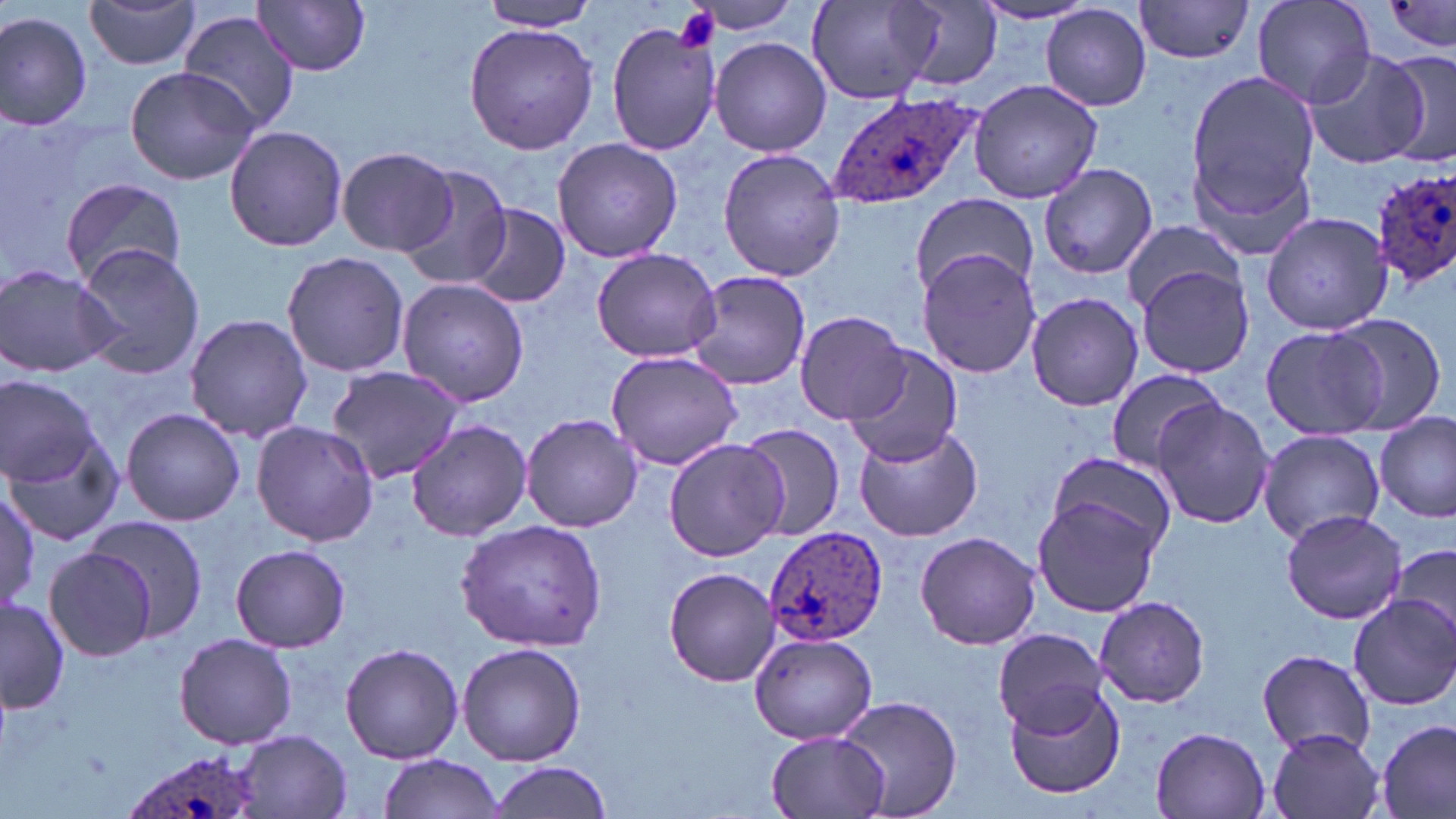 Approximate bounding boxes as (x1, y1, x2, y2) in pixels. Plasmodium ovale-infected red blood cell locations: (826, 89, 981, 213), (1373, 168, 1456, 285), (762, 524, 889, 646), (119, 746, 268, 819). Platelet locations: (675, 6, 721, 53). Uninfected red blood cell locations: (82, 0, 203, 70), (807, 0, 943, 106), (1134, 0, 1255, 64), (1252, 0, 1377, 108), (255, 1, 372, 75), (1381, 1, 1456, 51), (475, 2, 604, 31), (680, 2, 809, 37), (896, 2, 1004, 94), (973, 2, 1096, 25), (1041, 4, 1152, 111), (0, 8, 95, 131), (179, 9, 300, 135), (464, 23, 598, 156), (608, 23, 719, 156), (710, 36, 833, 157), (1300, 46, 1430, 168), (1379, 47, 1456, 162), (122, 64, 262, 186), (1185, 67, 1320, 219), (969, 77, 1104, 205), (223, 125, 347, 251), (551, 136, 684, 263), (336, 146, 457, 257), (718, 148, 846, 283), (395, 163, 514, 291), (1039, 164, 1158, 279), (59, 176, 188, 290), (909, 191, 1039, 299), (465, 203, 569, 309), (1261, 210, 1395, 335), (1120, 218, 1245, 315), (70, 243, 209, 381), (590, 247, 722, 363), (918, 249, 1042, 378), (282, 250, 409, 379), (0, 264, 121, 379), (1136, 265, 1253, 379), (683, 268, 812, 392), (397, 279, 529, 408), (1026, 290, 1143, 411), (795, 309, 912, 423), (184, 313, 313, 444), (1330, 314, 1450, 433), (1259, 323, 1390, 441), (843, 346, 963, 467), (606, 351, 742, 469), (326, 364, 464, 484), (1103, 369, 1226, 473), (1, 376, 100, 484), (1150, 399, 1275, 530), (121, 408, 245, 527), (521, 413, 643, 532), (1375, 413, 1455, 522), (404, 419, 533, 541), (252, 421, 379, 547), (853, 421, 987, 543), (737, 423, 844, 540), (7, 425, 123, 550), (1257, 429, 1386, 543), (664, 436, 788, 562), (1047, 452, 1177, 560), (0, 487, 45, 611), (1031, 496, 1161, 617), (1280, 507, 1408, 625), (83, 514, 210, 644), (455, 518, 610, 651), (913, 533, 1042, 651), (1380, 541, 1456, 651), (231, 542, 352, 653), (43, 545, 157, 663), (663, 567, 778, 685), (1345, 593, 1456, 711), (0, 596, 72, 715), (1093, 596, 1211, 709), (992, 628, 1108, 736), (174, 631, 297, 749), (750, 633, 877, 745), (456, 642, 586, 765), (339, 643, 464, 764), (1254, 647, 1377, 756), (1003, 681, 1127, 799), (836, 694, 962, 818), (1375, 717, 1455, 819), (1148, 725, 1273, 818), (1265, 728, 1387, 819), (231, 731, 352, 818), (766, 731, 888, 817), (376, 754, 508, 819), (485, 760, 615, 819). Slide-level diagnosis: Plasmodium ovale. Captured at 1000x magnification. Single field of view. Image is 1456×819 pixels. May-Grünwald-Giemsa stain. Light microscopy. Thin blood film.